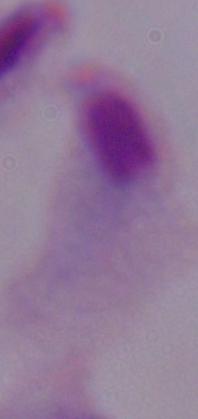 1000x magnification. Micrograph. A trichomonad is seen.